Outline each Plasmodium falciparum-infected red blood cell.
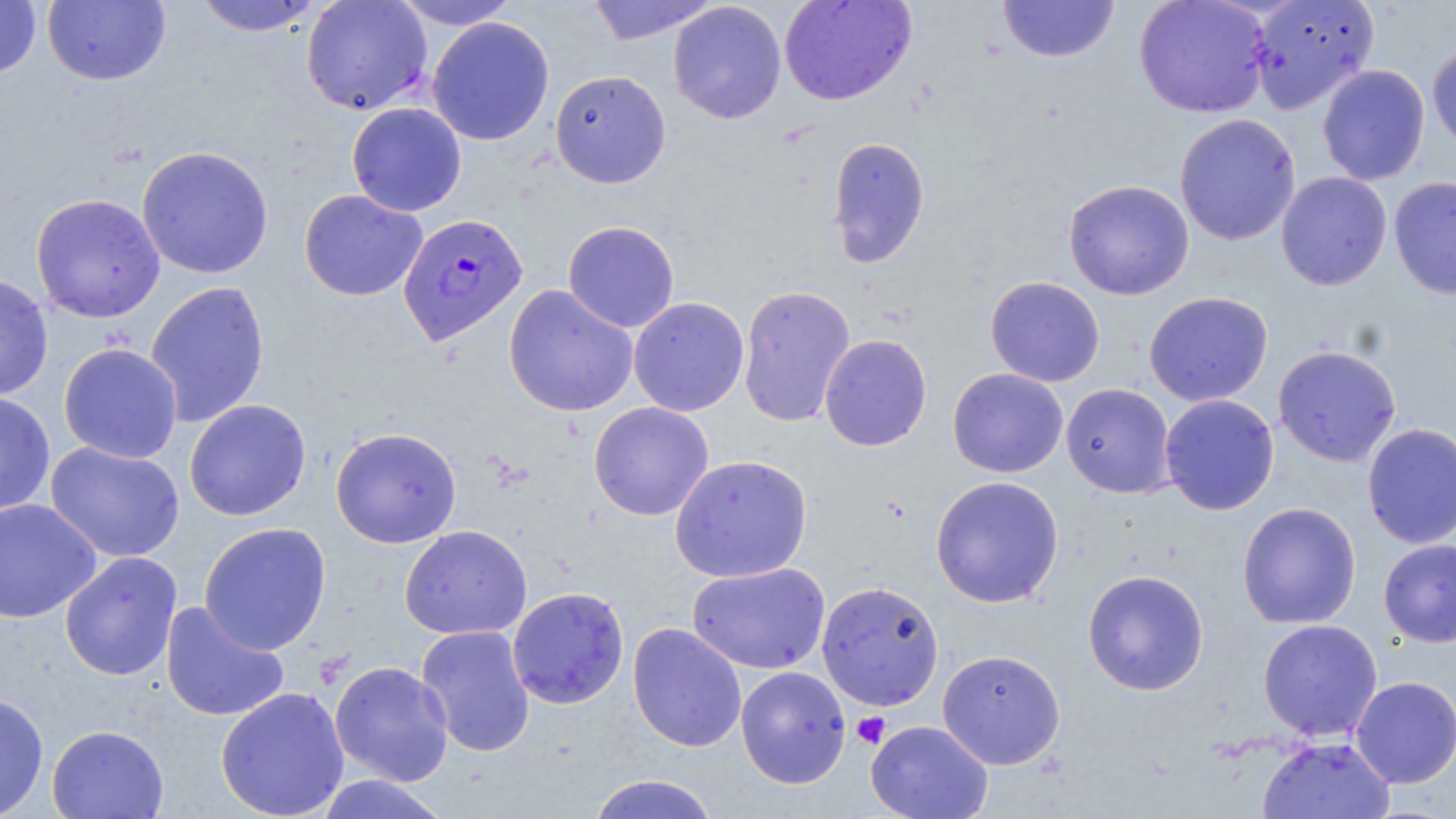

Approximate bounding boxes as (x1,y1)-(x2,y2) corner pairs in pixels.
Plasmodium falciparum-infected red blood cells: (397,212)-(528,346).

Uninfected red blood cell locations: (0,0)-(41,79), (42,0)-(171,86), (191,0)-(325,37), (301,0)-(433,116), (390,0)-(522,30), (586,0)-(721,45), (778,0)-(917,106), (997,0)-(1120,63), (1133,0)-(1272,119), (1247,1)-(1379,115), (668,2)-(787,124), (426,17)-(555,145), (1427,43)-(1456,158), (1317,65)-(1430,186), (549,69)-(671,188), (346,102)-(467,216), (1174,114)-(1301,246), (826,136)-(930,267), (136,145)-(274,279), (1276,171)-(1392,291), (1389,176)-(1456,300), (1063,179)-(1194,300), (299,189)-(427,301), (31,193)-(165,323), (562,220)-(680,333), (0,272)-(53,401), (985,275)-(1105,387), (145,281)-(270,428), (504,284)-(638,417), (737,285)-(856,428), (1143,291)-(1272,407), (628,297)-(749,416), (819,334)-(932,452), (58,343)-(183,464), (1273,345)-(1401,467), (947,368)-(1068,478), (1060,383)-(1175,499), (0,391)-(55,516), (1159,394)-(1279,515), (184,399)-(311,521), (588,401)-(714,522), (1362,422)-(1456,549), (330,427)-(462,548), (45,441)-(185,562), (669,454)-(813,583), (930,475)-(1064,607), (0,498)-(101,623), (1237,502)-(1361,629), (198,521)-(332,655), (399,524)-(532,640), (1378,540)-(1456,647), (59,551)-(182,681), (687,562)-(830,675), (1082,569)-(1209,695), (816,580)-(944,711), (507,586)-(629,710), (160,600)-(290,722), (1257,619)-(1383,741), (627,622)-(747,752), (415,625)-(536,757), (937,649)-(1066,769), (330,660)-(454,786), (735,666)-(851,789), (1350,676)-(1456,788), (215,686)-(349,819), (0,692)-(49,819), (866,719)-(993,819), (47,724)-(169,818), (1257,736)-(1395,819), (312,774)-(454,819), (586,774)-(722,819). Platelet locations: (852,712)-(890,749). Slide-level diagnosis: Plasmodium falciparum. 1000x magnification. Single field of view. May-Grünwald-Giemsa-stained preparation. Thin blood film. Light microscopy. Image is 1456×819 pixels.